Name the parasite shown.
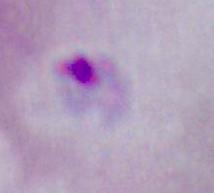
Plasmodium.

Summary:
  - Modality: photomicrograph
  - Magnification: 400x or 1000x